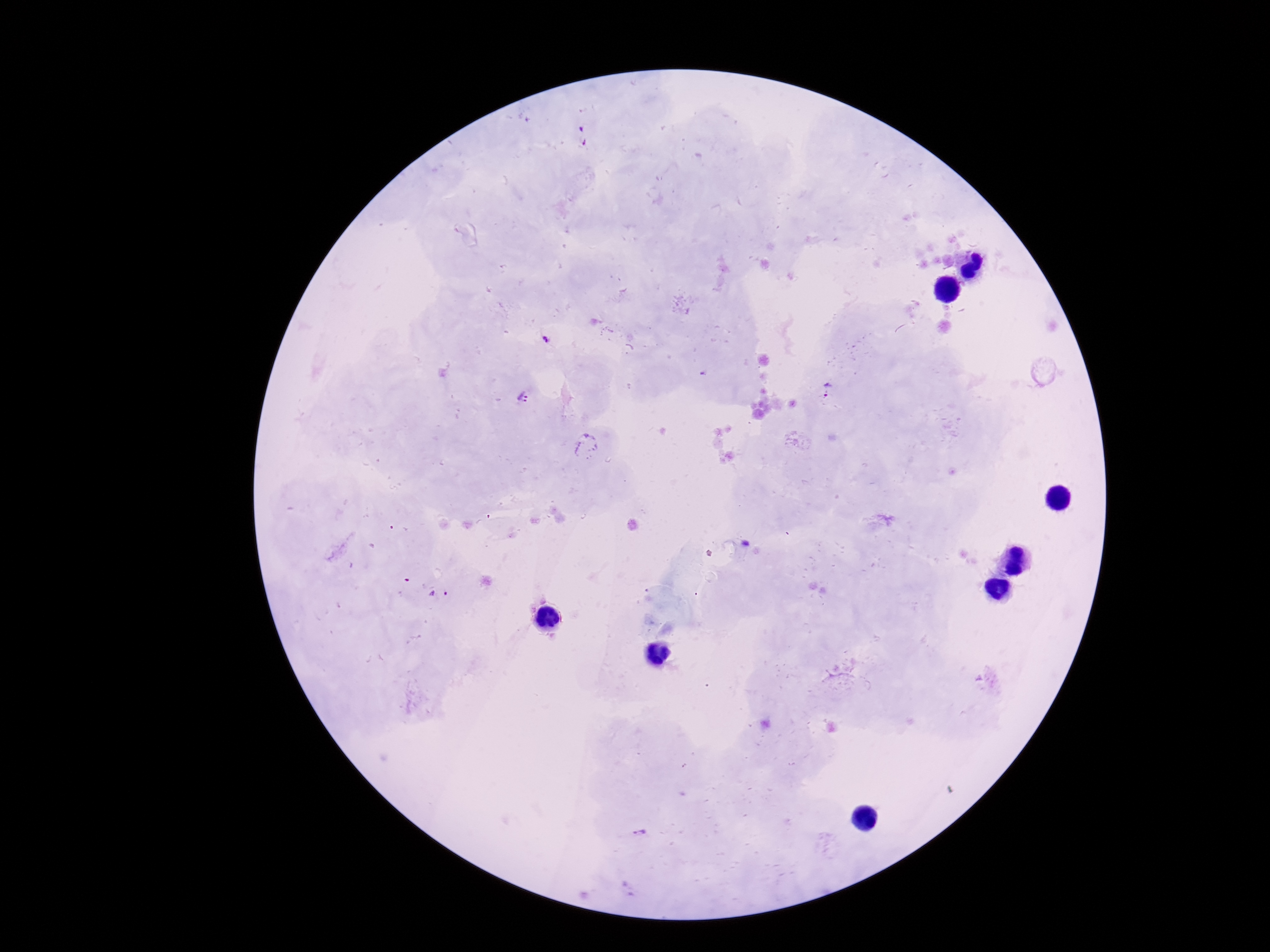

{
  "capture": "smartphone camera through the microscope eyepiece",
  "patient_malaria_status": "infected",
  "field_of_view": "one from this slide",
  "plasmodium_parasite_locations": "approximate object centers, in pixels from the top-left corner: (x=826, y=390), (x=523, y=398), (x=587, y=445), (x=438, y=593), (x=639, y=831), (x=629, y=888)",
  "stain": "Giemsa",
  "preparation": "thick blood film",
  "magnification": "100x",
  "image_size": "1270×952 pixels"
}